Assess the morphology of the erythrocytes.
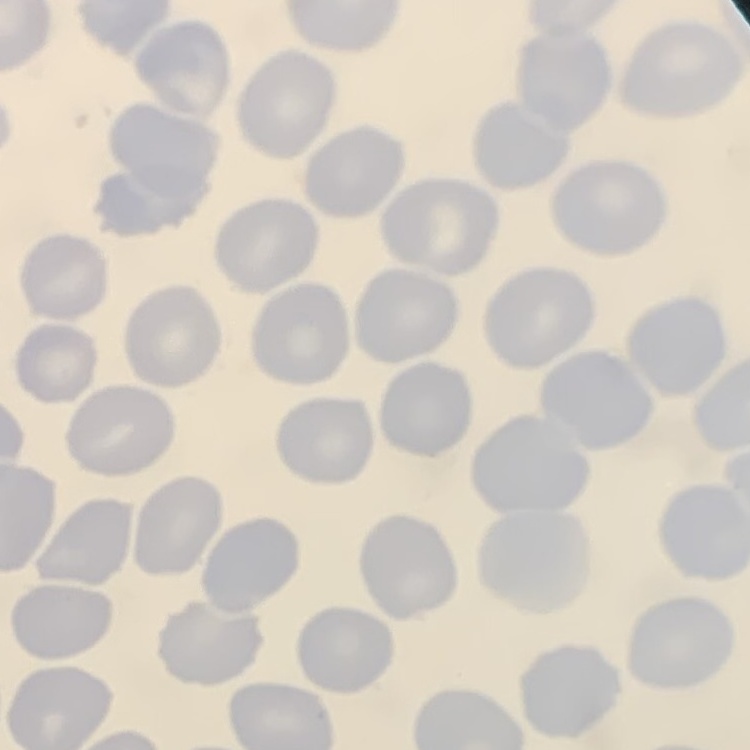
They show no rouleaux formation.

Thin peripheral smear. One tile cut from a larger photomicrograph. Field's or Giemsa stain.